Outline each uninfected red blood cell.
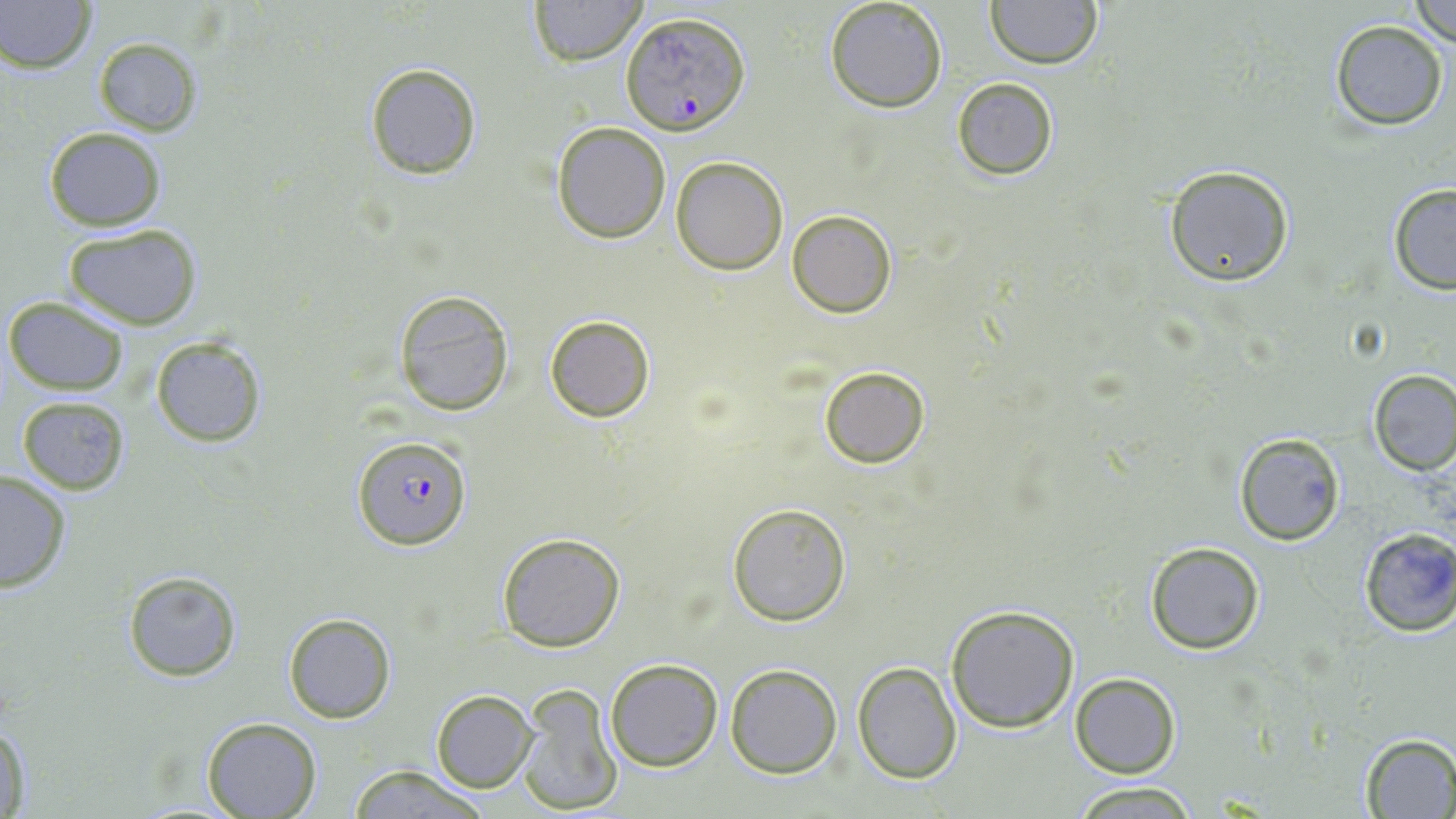
Approximate bounding boxes as (x1, y1, x2, y2) in pixels.
Uninfected red blood cells: (527, 0, 646, 66), (985, 0, 1103, 69), (0, 1, 95, 73), (1409, 1, 1456, 44), (823, 2, 947, 113), (1329, 20, 1449, 130), (92, 36, 203, 136), (364, 62, 482, 179), (951, 77, 1059, 182), (551, 121, 671, 243), (42, 127, 167, 230), (671, 156, 788, 274), (1162, 165, 1295, 286), (1387, 183, 1456, 295), (787, 208, 898, 318), (62, 224, 203, 329), (393, 292, 515, 417), (3, 296, 129, 396), (544, 315, 655, 422), (150, 335, 267, 446), (819, 365, 930, 469), (1368, 369, 1455, 475), (16, 395, 132, 494), (1234, 434, 1345, 545), (0, 471, 72, 595), (726, 502, 850, 625), (1357, 527, 1456, 636), (496, 532, 625, 651), (1144, 542, 1266, 655), (123, 571, 243, 681), (945, 605, 1080, 732), (281, 612, 396, 723), (604, 657, 723, 770), (851, 661, 963, 785), (725, 664, 842, 779), (1071, 672, 1180, 778), (516, 685, 622, 813), (432, 690, 536, 791), (202, 716, 321, 817), (1, 718, 34, 819), (1357, 733, 1456, 816), (346, 765, 492, 819), (1072, 782, 1199, 817).

slide_level_diagnosis: Plasmodium falciparum
field_of_view: single
plasmodium_falciparum_infected_red_blood_cell_locations: 'approximate bounding boxes as (x1, y1, x2, y2) in pixels: (622, 11, 750, 136), (352, 435, 472, 551)'
preparation: thin blood film
magnification: 1000x
image_size: 1456×819 pixels
stain: May-Grünwald-Giemsa
modality: optical microscopy